Outline each Plasmodium ovale-infected red blood cell.
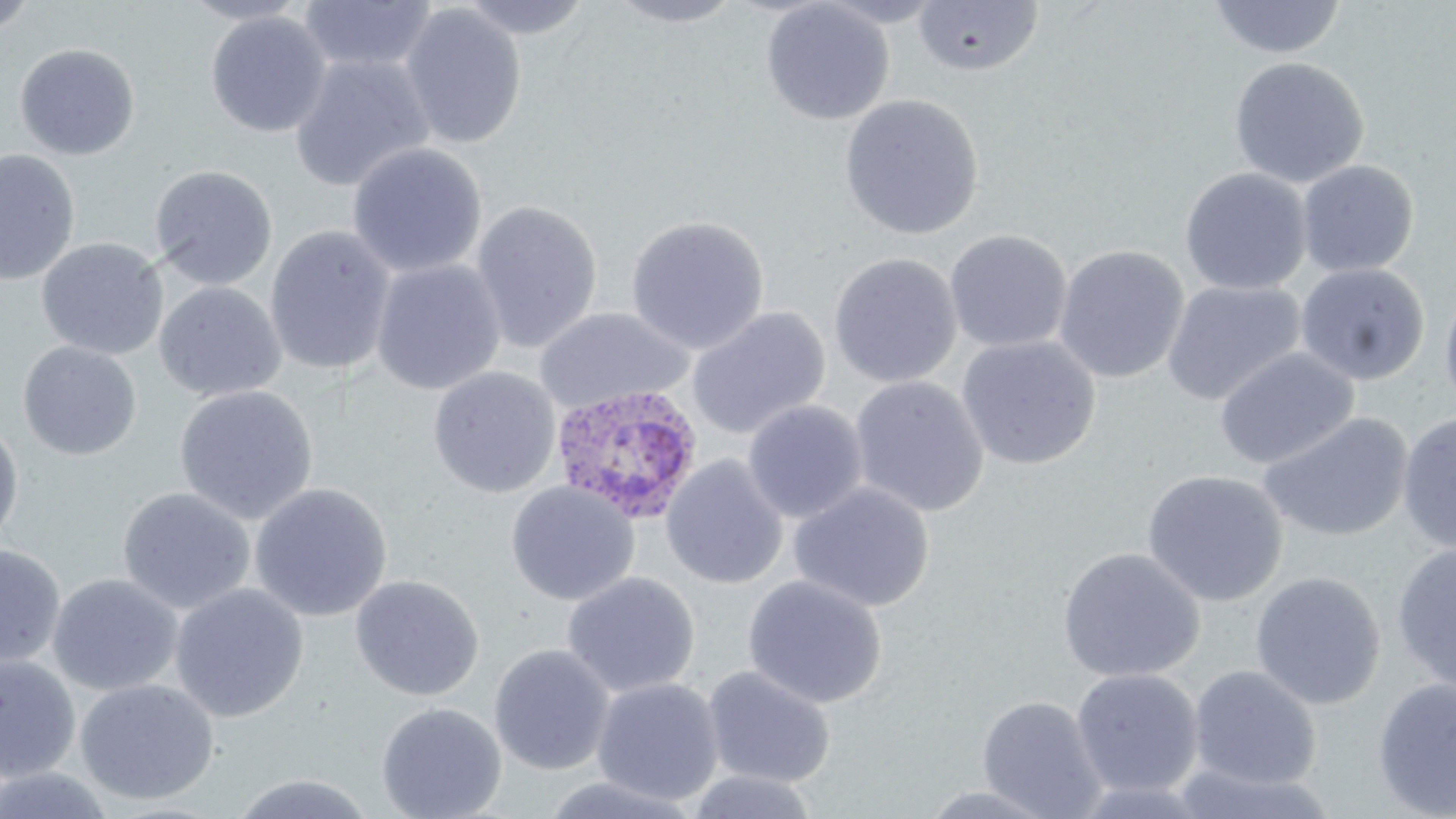
Approximate bounding boxes as [x1, y1, x2, y2] in pixels.
Plasmodium ovale-infected red blood cells: [550, 384, 705, 525].

slide-level diagnosis = Plasmodium ovale
uninfected red blood cell locations = approximate bounding boxes as [x1, y1, x2, y2] in pixels: [0, 0, 41, 40], [178, 0, 310, 26], [454, 0, 597, 40], [604, 0, 748, 28], [1207, 0, 1347, 60], [298, 1, 438, 75], [761, 1, 895, 126], [911, 2, 1046, 77], [400, 4, 527, 150], [205, 11, 331, 138], [14, 42, 140, 161], [288, 53, 436, 193], [1228, 56, 1369, 188], [839, 93, 985, 240], [347, 142, 488, 277], [0, 149, 80, 286], [1296, 160, 1419, 278], [149, 164, 278, 290], [1179, 167, 1312, 295], [470, 199, 604, 352], [625, 214, 769, 354], [263, 224, 397, 377], [944, 229, 1073, 353], [36, 238, 169, 360], [1053, 244, 1190, 384], [828, 252, 962, 389], [370, 259, 506, 395], [1294, 262, 1430, 386], [1438, 278, 1456, 418], [1161, 279, 1307, 407], [154, 281, 286, 402], [533, 306, 694, 414], [686, 306, 831, 440], [956, 335, 1101, 470], [18, 341, 142, 461], [1215, 347, 1358, 470], [427, 367, 561, 498], [849, 375, 990, 517], [174, 384, 319, 524], [742, 400, 868, 523], [1397, 411, 1456, 554], [1258, 412, 1414, 543], [0, 416, 24, 553], [661, 454, 789, 590], [1141, 469, 1288, 607], [505, 481, 640, 606], [249, 482, 393, 621], [788, 482, 935, 612], [117, 486, 256, 615], [1391, 542, 1456, 695], [0, 544, 66, 670], [1056, 547, 1206, 683], [1249, 570, 1386, 710], [562, 571, 701, 697], [47, 573, 183, 697], [349, 574, 485, 701], [743, 574, 887, 709], [170, 583, 308, 723], [489, 643, 615, 775], [0, 654, 81, 781], [1187, 664, 1322, 790], [702, 665, 837, 787], [1071, 667, 1204, 798], [591, 677, 724, 806], [1372, 677, 1456, 819], [75, 678, 220, 805], [977, 695, 1107, 818], [376, 701, 507, 819], [1167, 763, 1341, 819], [0, 767, 118, 818], [684, 769, 821, 819], [227, 773, 380, 818], [537, 774, 705, 818], [916, 784, 1062, 818]
preparation = thin blood smear
magnification = 1000x
image size = 1456×819 pixels
field of view = single
modality = light microscopy
stain = May-Grünwald-Giemsa